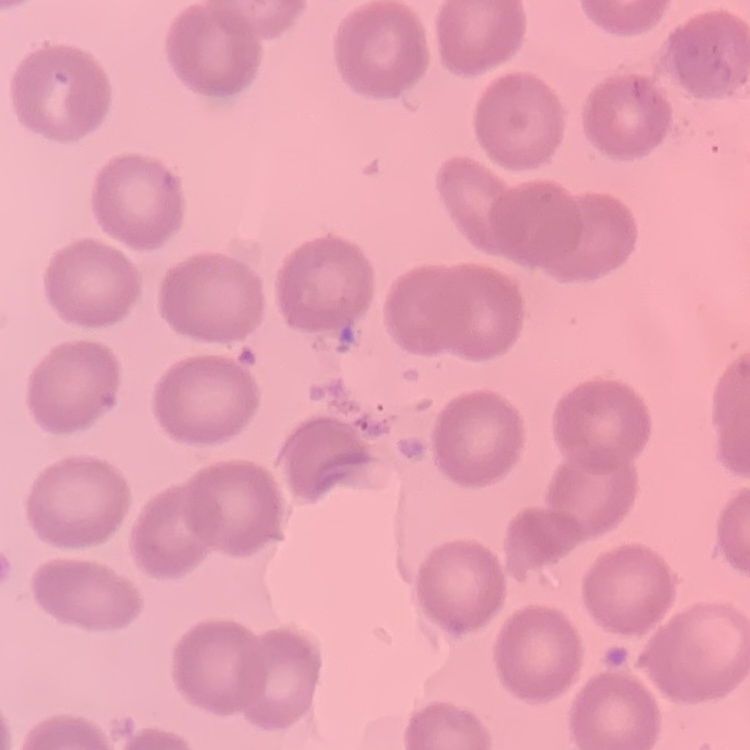

Summary:
  - Red blood cell morphology: no rouleaux formation
  - Stain: Field's or Giemsa
  - Image type: square crop of a larger photomicrograph
  - Preparation: thin blood smear